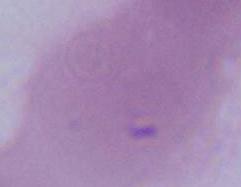

Summary:
  - Modality: micrograph
  - Identification: red blood cell
  - Magnification: 1000x